Assess this cell for malaria.
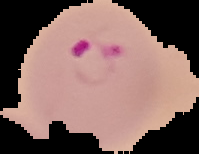
Parasitized.

Summary:
  - Image size: 199×154 pixels
  - Preparation: thin blood film
  - Image type: segmented cell region with the area outside set to black